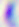
{
  "modality": "micrograph",
  "identification": "Toxoplasma gondii",
  "magnification": "400x"
}